Evaluate for Plasmodium parasites.
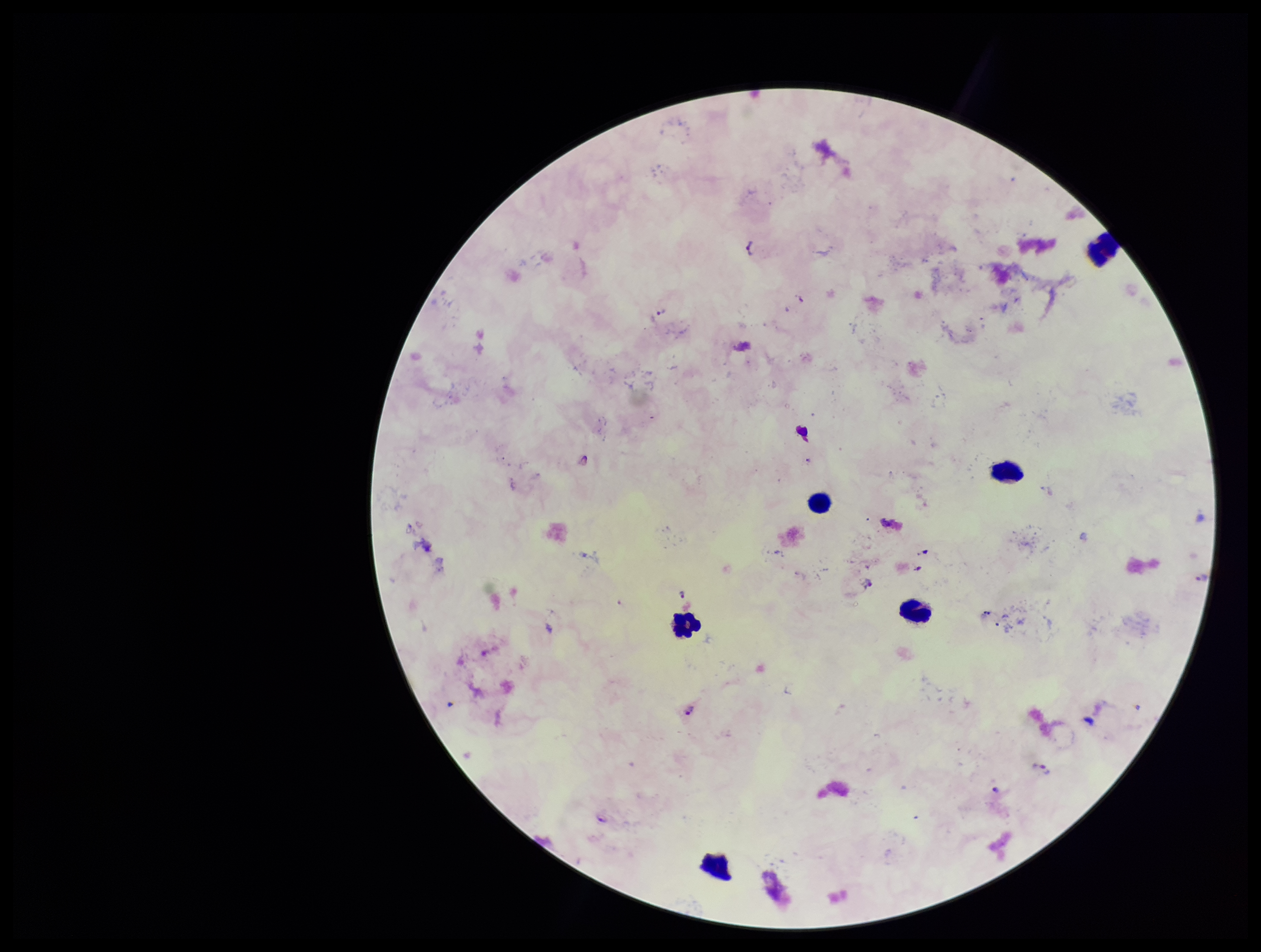

Seen.

species reported for this patient = Plasmodium falciparum
parasite count = 5
image size = 1261×952 pixels
stain = Giemsa
capture = smartphone photograph through the microscope eyepiece
field of view = one from this slide
patient malaria status = positive
preparation = thick smear
leukocyte count = 6